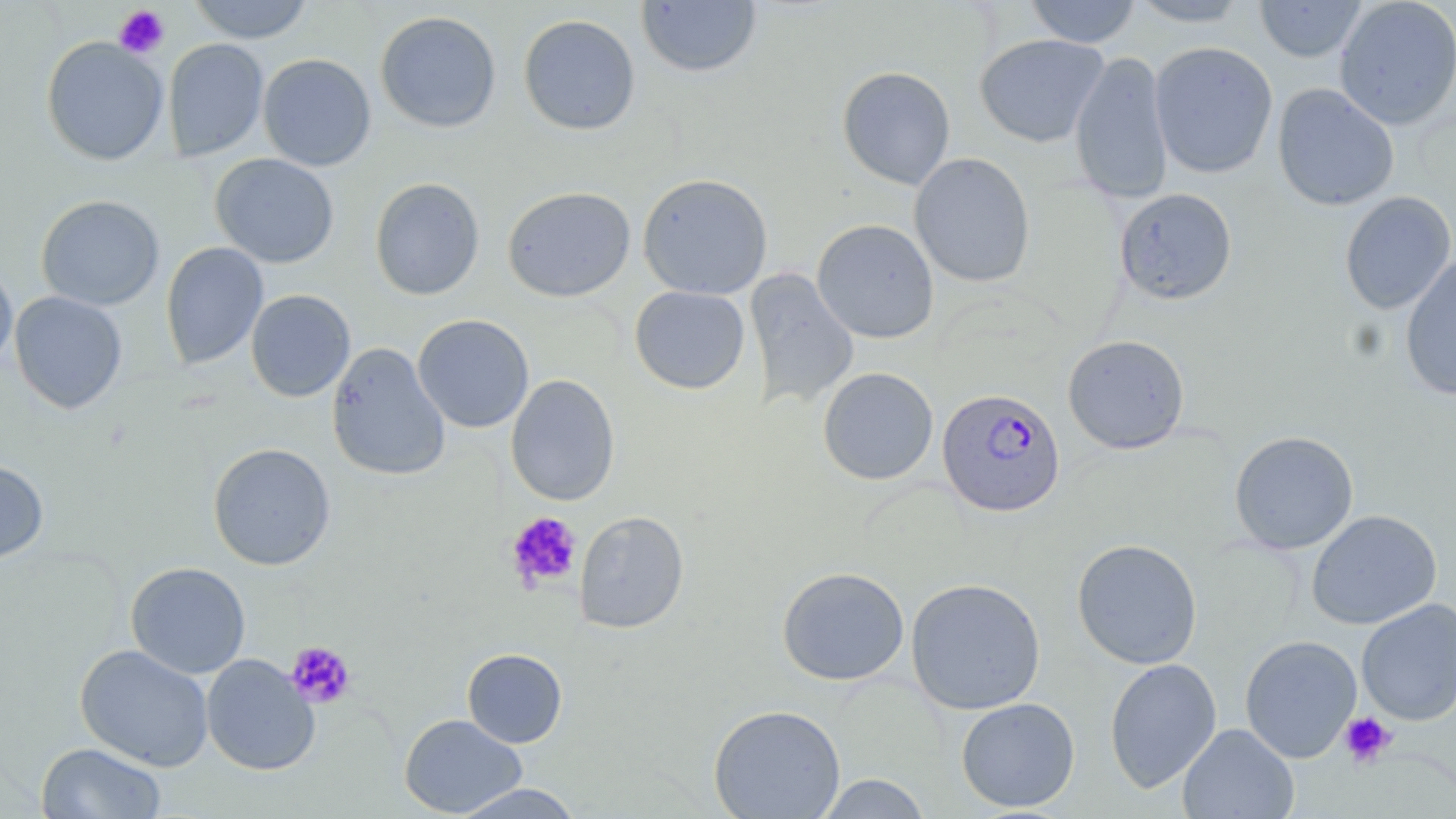
Approximate bounding boxes as (x1, y1, x2, y2) in pixels. Platelet locations: (114, 5, 169, 59), (506, 512, 582, 591), (285, 641, 356, 708), (1338, 711, 1397, 768). Uninfected red blood cell locations: (187, 0, 315, 44), (636, 0, 762, 78), (1024, 0, 1142, 47), (1127, 0, 1252, 26), (1333, 0, 1456, 130), (1254, 1, 1368, 63), (375, 10, 501, 133), (518, 14, 640, 135), (973, 33, 1109, 148), (41, 36, 169, 166), (163, 39, 269, 162), (1149, 41, 1278, 179), (1070, 51, 1173, 204), (258, 53, 376, 171), (837, 66, 956, 190), (1272, 83, 1399, 211), (909, 152, 1035, 288), (210, 153, 339, 268), (637, 173, 774, 300), (370, 177, 485, 300), (502, 186, 636, 302), (1114, 187, 1237, 305), (1339, 191, 1456, 314), (35, 194, 164, 311), (812, 218, 939, 343), (161, 242, 268, 370), (1400, 255, 1456, 402), (0, 260, 18, 375), (744, 268, 859, 411), (629, 286, 750, 394), (245, 289, 356, 402), (10, 291, 128, 414), (412, 314, 534, 433), (1062, 334, 1190, 454), (327, 342, 451, 481), (817, 367, 938, 485), (505, 374, 620, 505), (1229, 430, 1359, 555), (208, 442, 336, 571), (0, 460, 49, 562), (1306, 509, 1442, 629), (573, 511, 689, 633), (1071, 538, 1203, 669), (1091, 538, 1210, 793), (125, 562, 251, 678), (776, 566, 909, 686), (905, 577, 1046, 715), (1356, 598, 1456, 725), (1240, 635, 1361, 763), (74, 644, 214, 771), (462, 648, 568, 748), (202, 654, 320, 775), (1104, 658, 1222, 793), (956, 697, 1080, 812), (708, 703, 846, 819), (399, 713, 527, 817), (1177, 723, 1299, 819), (36, 742, 166, 819), (815, 773, 932, 818), (450, 783, 584, 818). Plasmodium falciparum-infected red blood cell locations: (936, 387, 1066, 517). Slide-level diagnosis: Plasmodium falciparum. Optical microscopy. Thin blood film. One field of a larger specimen. 1000x magnification. Image is 1456×819 pixels. May-Grünwald-Giemsa stain.